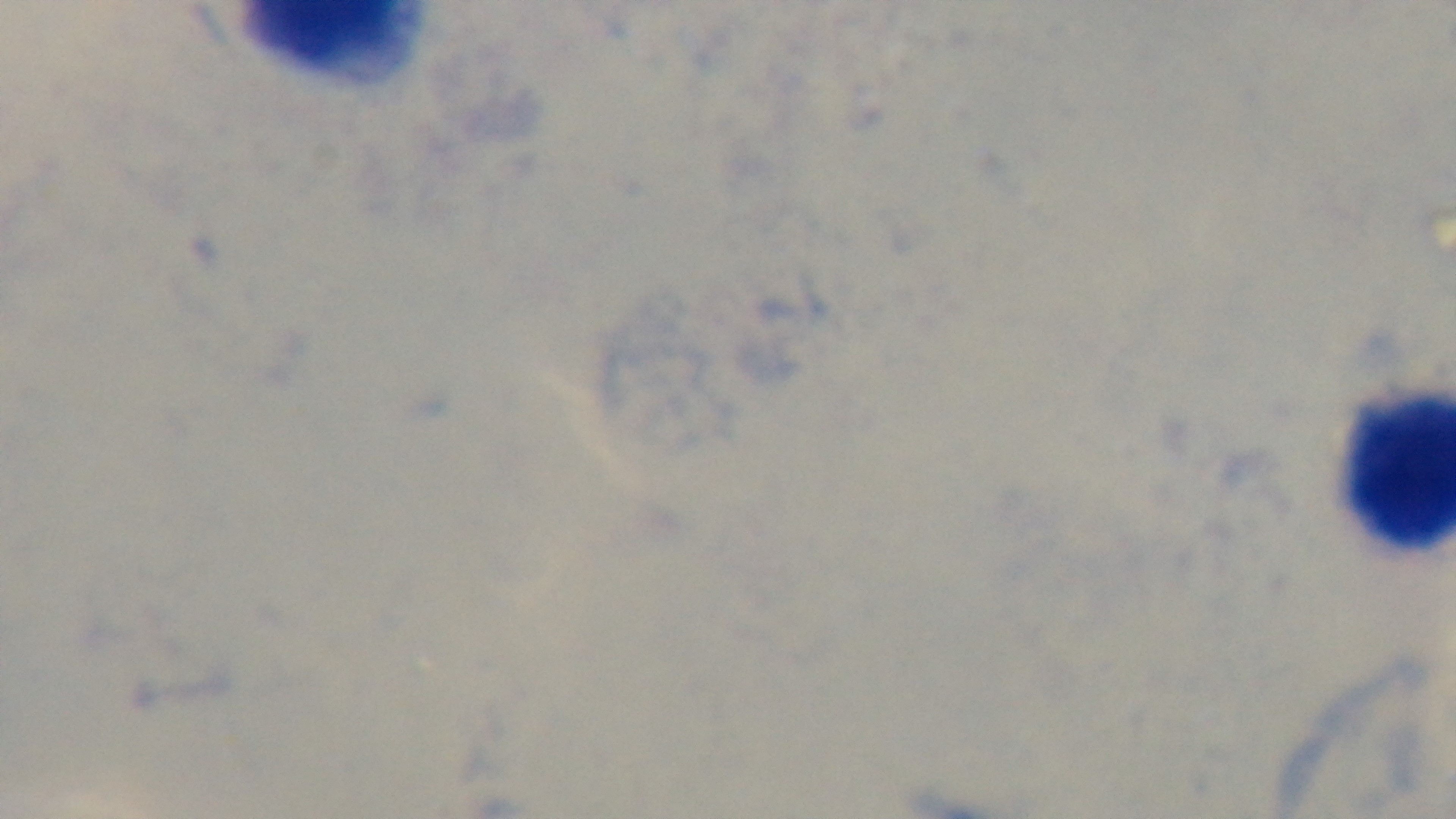
Summary:
  - Preparation: thick blood film
  - Modality: light microscopy
  - Field of view: one from the slide
  - Stain: Giemsa
  - Objective: 100x oil immersion
  - Malaria status: negative
  - Capture: mounted 4K digital camera